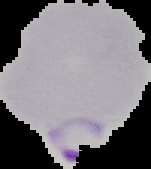

Image is 151×169 pixels. From a thin blood film. The area outside the segmented cell region is set to black. Result: Plasmodium parasites detected.